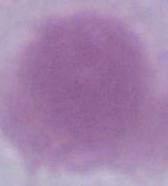

Summary:
  - Magnification: 1000x
  - Modality: photomicrograph
  - Identification: red blood cell